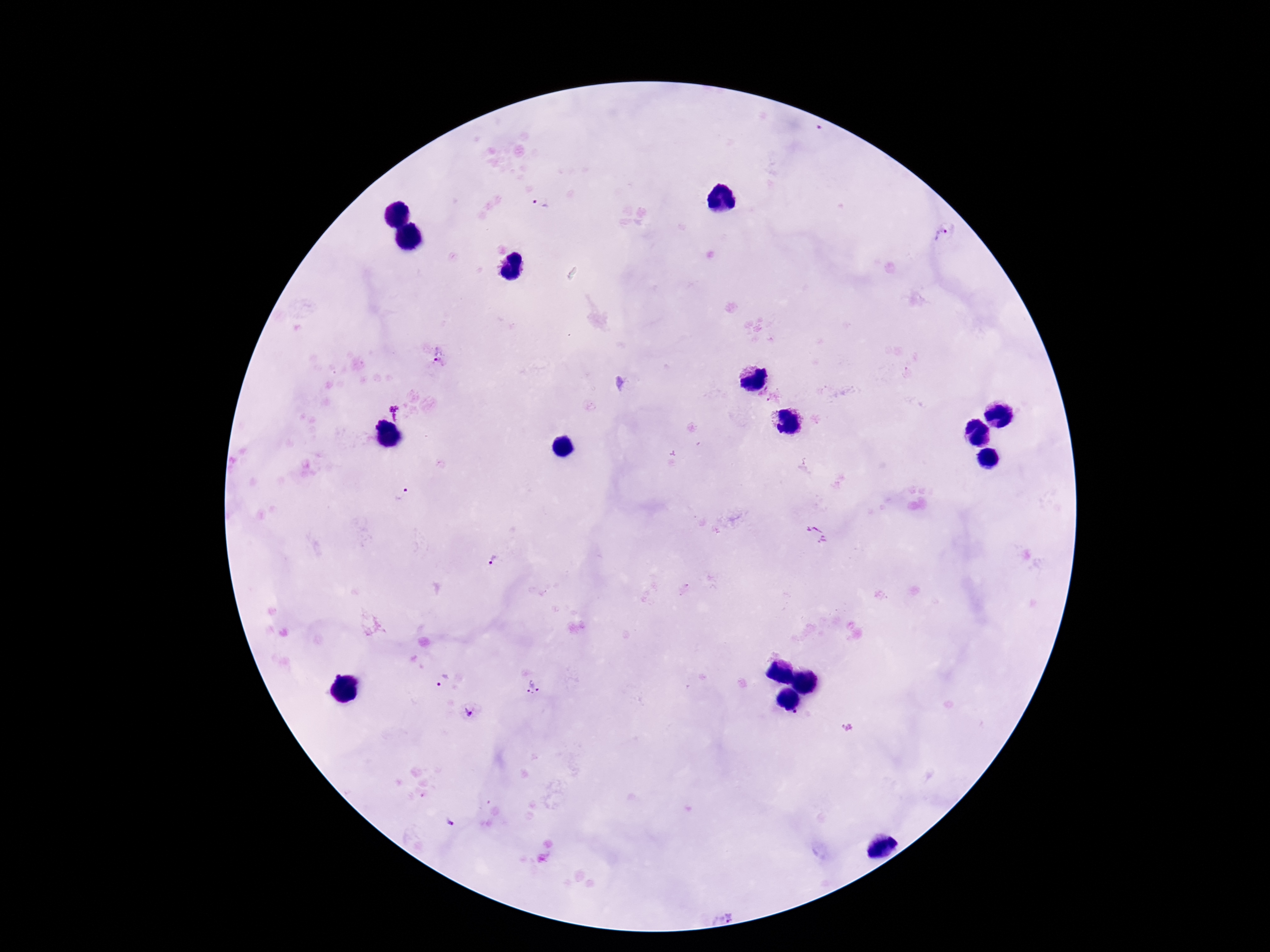
Approximate centers as (x, y) in pixels. Plasmodium parasite locations: (543, 204), (944, 236), (441, 356), (394, 414), (402, 495), (817, 535), (495, 563), (443, 681), (533, 688), (468, 711), (799, 716), (847, 727), (450, 823), (724, 915). Thick blood smear. Patient malaria status: positive. Giemsa-stained preparation. Smartphone photograph taken through the microscope eyepiece. 100x magnification. Single field of view. Image is 1270×952 pixels.